Describe the morphology of the red blood cells.
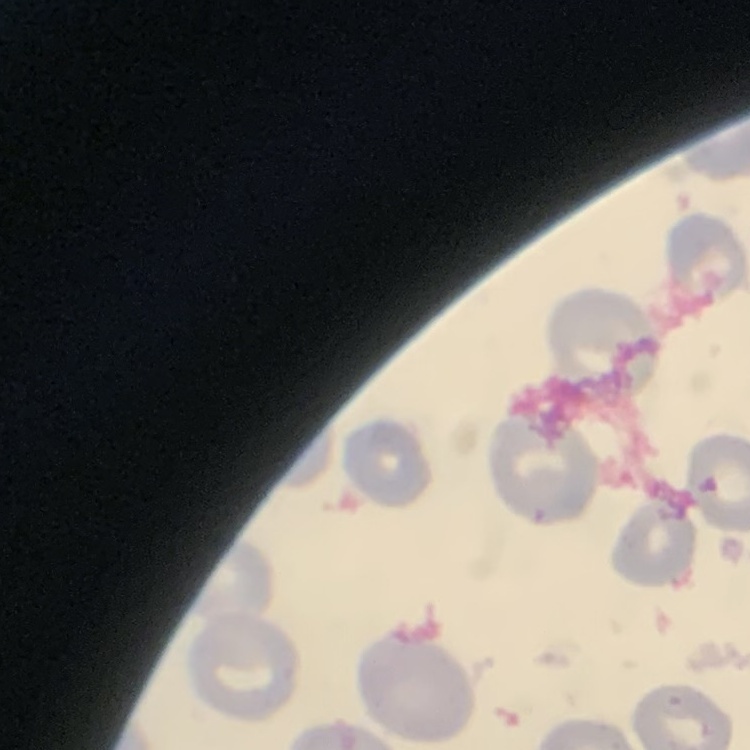

They show no rouleaux formation.

Field's or Giemsa stain. Square crop of a larger photomicrograph. Thin blood smear.